Identify the blood parasite species.
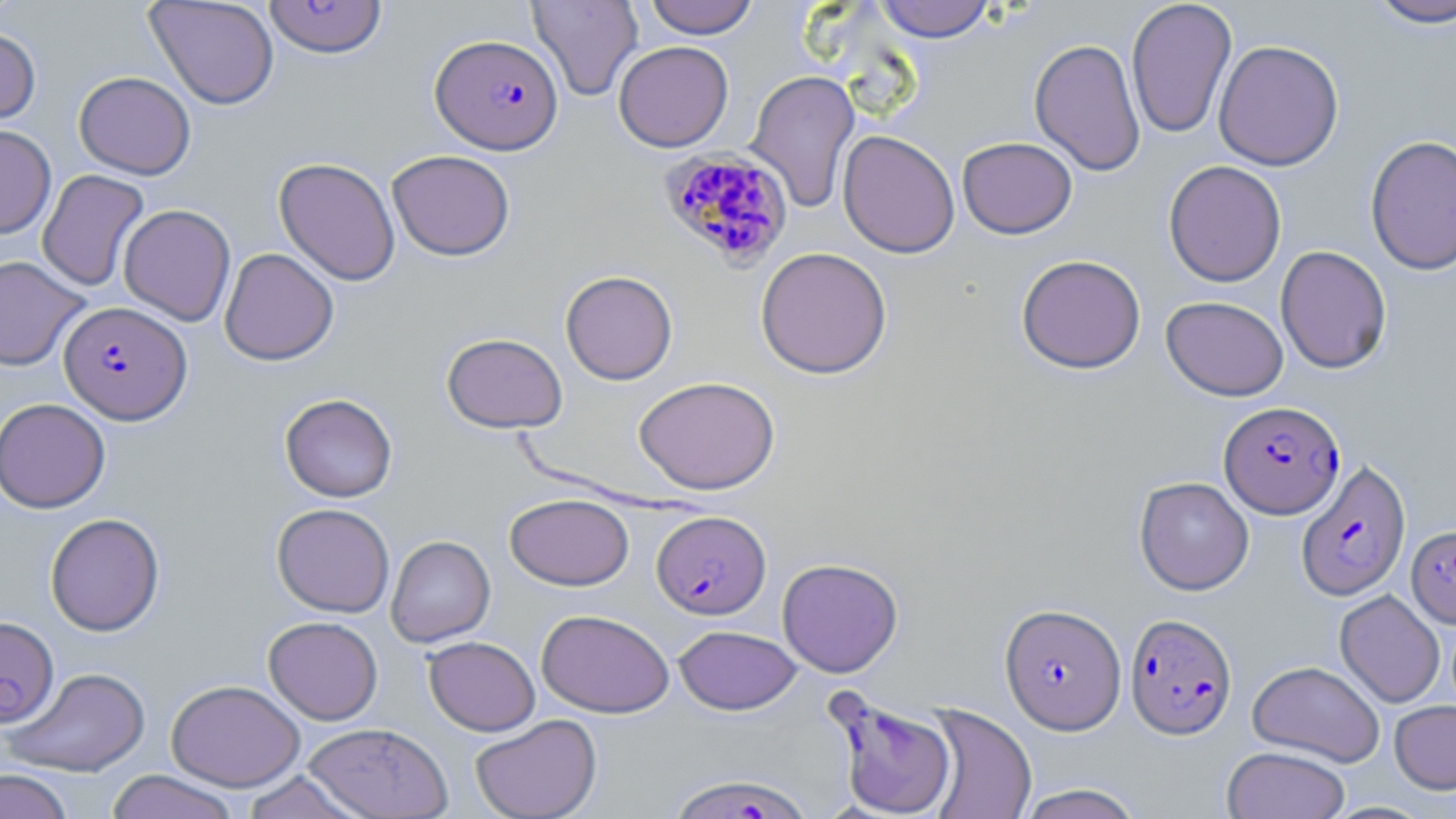
Plasmodium falciparum.

field of view = single
preparation = thin blood film
image size = 1456×819 pixels
modality = optical microscopy
magnification = 1000x
uninfected red blood cell locations (subset) = approximate bounding boxes as named x1/y1/x2/y2 corners in pixels: (x1=0, y1=0, x2=24, y2=28), (x1=144, y1=0, x2=280, y2=110), (x1=527, y1=0, x2=644, y2=101), (x1=643, y1=0, x2=759, y2=38), (x1=873, y1=0, x2=997, y2=42), (x1=1125, y1=0, x2=1237, y2=140), (x1=1363, y1=0, x2=1456, y2=29), (x1=0, y1=28, x2=41, y2=125), (x1=1029, y1=38, x2=1146, y2=176), (x1=1213, y1=39, x2=1344, y2=170), (x1=613, y1=40, x2=734, y2=152), (x1=746, y1=69, x2=861, y2=213), (x1=74, y1=71, x2=196, y2=179), (x1=0, y1=124, x2=56, y2=238), (x1=838, y1=129, x2=960, y2=258), (x1=1365, y1=135, x2=1456, y2=275), (x1=957, y1=136, x2=1077, y2=239), (x1=387, y1=150, x2=515, y2=261), (x1=274, y1=157, x2=400, y2=286), (x1=1163, y1=160, x2=1287, y2=287), (x1=37, y1=169, x2=150, y2=292), (x1=118, y1=204, x2=236, y2=326), (x1=1275, y1=245, x2=1393, y2=374), (x1=755, y1=246, x2=892, y2=379), (x1=219, y1=248, x2=339, y2=365), (x1=1016, y1=254, x2=1147, y2=374), (x1=0, y1=256, x2=89, y2=371), (x1=560, y1=270, x2=678, y2=385), (x1=1161, y1=296, x2=1289, y2=401), (x1=441, y1=332, x2=568, y2=433), (x1=633, y1=375, x2=780, y2=495), (x1=279, y1=393, x2=398, y2=502), (x1=0, y1=397, x2=111, y2=513), (x1=1134, y1=476, x2=1254, y2=595), (x1=505, y1=493, x2=634, y2=591), (x1=271, y1=503, x2=395, y2=617), (x1=45, y1=513, x2=165, y2=636), (x1=386, y1=535, x2=496, y2=647), (x1=777, y1=557, x2=903, y2=678), (x1=1335, y1=590, x2=1446, y2=707), (x1=536, y1=609, x2=674, y2=717), (x1=263, y1=616, x2=383, y2=725), (x1=673, y1=624, x2=802, y2=715), (x1=423, y1=636, x2=540, y2=736), (x1=1247, y1=660, x2=1385, y2=767), (x1=4, y1=667, x2=151, y2=777), (x1=166, y1=679, x2=304, y2=791), (x1=1389, y1=699, x2=1456, y2=794), (x1=921, y1=704, x2=1037, y2=819), (x1=470, y1=713, x2=602, y2=819), (x1=302, y1=722, x2=452, y2=818), (x1=1222, y1=745, x2=1351, y2=819), (x1=0, y1=768, x2=75, y2=818), (x1=105, y1=770, x2=241, y2=819), (x1=239, y1=770, x2=368, y2=819), (x1=1014, y1=784, x2=1145, y2=819)
stain = May-Grünwald-Giemsa
Plasmodium falciparum-infected red blood cell locations (subset) = approximate bounding boxes as named x1/y1/x2/y2 corners in pixels: (x1=431, y1=33, x2=564, y2=154), (x1=658, y1=148, x2=796, y2=269), (x1=59, y1=301, x2=191, y2=424), (x1=1218, y1=401, x2=1345, y2=518), (x1=1297, y1=459, x2=1410, y2=601), (x1=652, y1=510, x2=771, y2=619), (x1=1407, y1=525, x2=1456, y2=628), (x1=1000, y1=603, x2=1126, y2=734), (x1=1125, y1=613, x2=1237, y2=739), (x1=0, y1=616, x2=59, y2=728), (x1=827, y1=692, x2=958, y2=818), (x1=666, y1=772, x2=813, y2=818)